Locate the cells, classifying each as a parasitized RBC, an uninfected RBC, or a WBC.
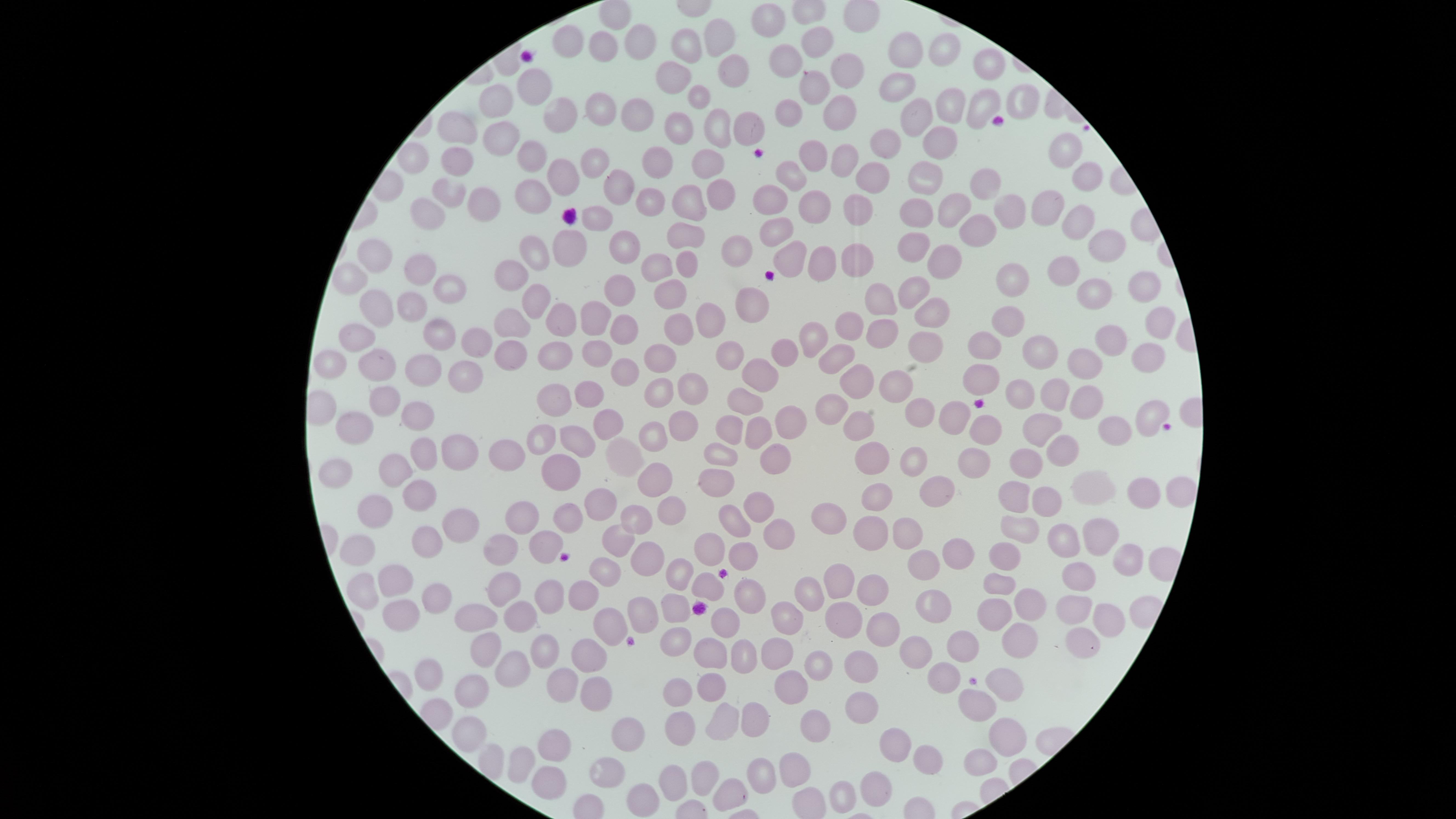

No parasitized RBCs identified.
Approximate marker points as [x, y] in pixels.
Uninfected RBCs: [613, 11], [770, 18], [715, 35], [563, 40], [819, 42], [632, 43], [688, 44], [605, 48], [910, 48], [951, 49], [788, 57], [730, 63], [990, 65], [848, 68], [673, 76], [535, 82], [814, 86], [899, 86], [697, 93], [495, 95], [955, 98], [1022, 100], [838, 102], [981, 103], [596, 104], [635, 110], [561, 112], [918, 113], [788, 114], [739, 123], [457, 124], [681, 126], [498, 128], [715, 131], [939, 136], [882, 140], [1064, 149], [532, 151], [813, 157], [847, 157], [412, 159], [459, 160], [658, 160], [708, 160], [592, 161], [922, 170], [873, 174], [563, 177], [791, 177], [1080, 181], [986, 185], [448, 189], [612, 189], [722, 195], [773, 198], [539, 200], [686, 200], [916, 202], [648, 203], [814, 203], [481, 206], [955, 206], [1046, 206], [1014, 209], [432, 210], [863, 210], [598, 217], [1081, 222], [779, 224], [980, 229], [685, 231], [623, 241], [918, 241], [1103, 245], [738, 246], [534, 247], [567, 250], [859, 254], [378, 256], [939, 257], [787, 258], [819, 258], [690, 261], [654, 266], [423, 270], [514, 270], [1059, 272], [349, 276], [1012, 276], [619, 281], [1145, 283], [450, 285], [912, 287], [1088, 289], [670, 294], [884, 298], [538, 300], [752, 304], [375, 306], [411, 306], [934, 314], [590, 315], [1014, 317], [557, 318], [708, 318], [515, 320], [622, 323], [847, 323], [673, 325], [1160, 328], [881, 332], [439, 333], [359, 334], [987, 341], [1103, 341], [812, 344], [934, 344], [474, 345], [727, 347], [558, 348], [1036, 350], [591, 352], [779, 353], [508, 354], [837, 354], [656, 355], [1143, 355], [334, 357], [376, 364], [411, 364], [1074, 364], [619, 366], [760, 370], [459, 372], [980, 377], [856, 382], [896, 383], [685, 386], [658, 389], [1013, 389], [591, 391], [1051, 391], [550, 394], [386, 396], [739, 397], [1080, 399], [828, 402], [919, 414], [1155, 414], [783, 416], [418, 417], [955, 417], [861, 423], [1048, 423], [611, 424], [678, 425], [987, 427], [349, 428], [731, 431], [759, 431], [1113, 432], [537, 437], [577, 437], [656, 438], [1063, 447], [456, 448], [425, 449], [506, 453], [722, 453], [876, 453], [626, 455], [774, 455], [1029, 458], [969, 460], [916, 462], [386, 465], [560, 470], [333, 473], [648, 478], [719, 484], [1098, 484], [1175, 488], [412, 490], [928, 490], [1017, 490], [1147, 493], [874, 496], [760, 500], [1047, 500], [597, 501], [664, 511], [378, 513], [831, 513], [568, 518], [459, 520], [634, 520], [518, 522], [732, 522], [1016, 522], [774, 528], [870, 530], [906, 530], [1097, 534], [426, 538], [1061, 538], [619, 541], [547, 545], [358, 547], [709, 547], [494, 553], [741, 553], [1117, 553], [642, 556], [949, 556], [1004, 558], [1080, 567], [602, 570], [684, 570], [918, 570], [394, 573], [845, 579], [705, 582], [998, 582], [493, 586], [358, 587], [582, 590], [747, 591], [874, 591], [816, 592], [435, 594], [545, 595], [931, 603], [1027, 604], [640, 611], [1071, 611], [390, 612], [461, 612], [674, 613], [993, 613], [783, 614], [519, 617], [850, 619], [604, 621], [1101, 621], [885, 625], [720, 626], [1084, 638], [1017, 640], [677, 641], [486, 644], [960, 644], [544, 650], [594, 653], [770, 653], [913, 653], [709, 654], [742, 658], [519, 659], [818, 663], [859, 666], [943, 673], [432, 676], [559, 680], [1001, 681], [792, 686], [718, 687], [594, 689], [474, 690], [681, 690], [972, 707], [865, 709], [748, 716], [719, 723], [817, 727], [685, 729], [467, 736], [1002, 739], [893, 741], [554, 742], [626, 744], [975, 758], [514, 761], [927, 761], [792, 765], [606, 773], [702, 774], [760, 774], [548, 779], [669, 781], [874, 787], [722, 791], [843, 792], [637, 794].
No WBCs identified.

{
  "image_size": "1456×819 pixels",
  "preparation": "thin blood film",
  "visible_region": "circular",
  "capture": "smartphone photograph through the microscope eyepiece",
  "field_of_view": "single",
  "stain": "Giemsa"
}